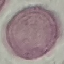
Malaria status: uninfected. Photographed with a smartphone camera at the microscope eyepiece. Giemsa-stained preparation. Thin blood smear. Cell patch, automatically extracted from a larger field of view and resized to 64 × 64 pixels.